Outline every malaria parasite.
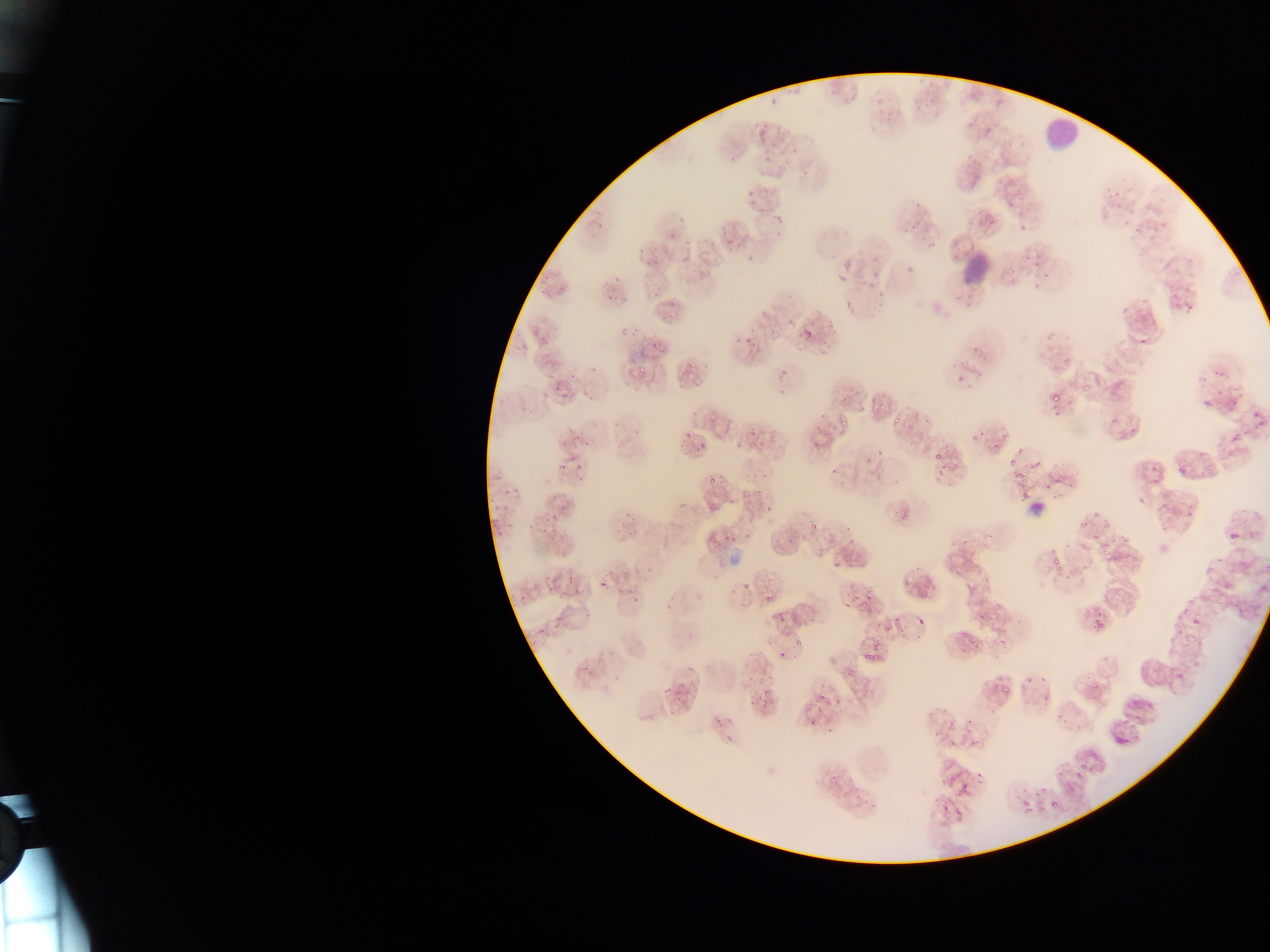
Approximate bounding boxes as (left, top, right, bottom) in pixels.
Malaria parasites: (870, 271, 881, 279), (521, 343, 527, 351), (547, 374, 555, 382), (1083, 380, 1094, 392), (1053, 394, 1065, 402), (1053, 406, 1065, 420), (836, 410, 848, 419), (894, 418, 905, 429), (1004, 433, 1011, 443), (750, 441, 756, 449), (1015, 444, 1026, 453), (876, 449, 887, 457), (933, 450, 943, 459), (1009, 454, 1018, 469), (948, 460, 959, 474), (936, 468, 943, 481), (1013, 471, 1027, 481), (720, 477, 726, 485), (1020, 493, 1030, 504), (758, 500, 767, 507), (763, 503, 772, 514), (901, 515, 911, 524), (810, 520, 816, 530), (1103, 521, 1112, 535), (724, 527, 730, 544), (742, 530, 752, 538), (847, 538, 855, 543), (817, 544, 825, 555), (1103, 548, 1111, 560), (1053, 557, 1066, 565), (1081, 563, 1088, 571), (599, 583, 609, 586), (995, 601, 1003, 610), (846, 603, 854, 611), (984, 613, 996, 625), (771, 614, 784, 625), (1172, 621, 1182, 631), (885, 628, 894, 635), (969, 635, 975, 643), (1000, 636, 1007, 646), (872, 643, 879, 654), (780, 650, 786, 658), (862, 654, 877, 661), (992, 681, 1003, 689), (764, 690, 772, 699), (817, 693, 827, 701), (835, 698, 841, 708), (967, 726, 973, 734), (969, 739, 982, 747), (1076, 763, 1088, 770), (975, 770, 986, 786), (1040, 787, 1048, 793), (1020, 797, 1031, 808), (942, 800, 954, 811), (1050, 800, 1059, 808), (1024, 807, 1036, 814) | approximate (x, y) pixel centers of objects too small to bound: (689, 365), (641, 371), (843, 423), (703, 446), (713, 480), (746, 493), (745, 587), (767, 596), (795, 635), (536, 641), (797, 642), (970, 649), (851, 779).

Summary:
  - Leukocyte locations: (1037, 109, 1091, 145), (958, 239, 1009, 285)
  - Field of view: single
  - Country: Ghana
  - Capture: mobile-phone photograph through a microscope
  - Image size: 1270×952 pixels
  - Preparation: thin blood film